Describe the morphology of the red blood cells.
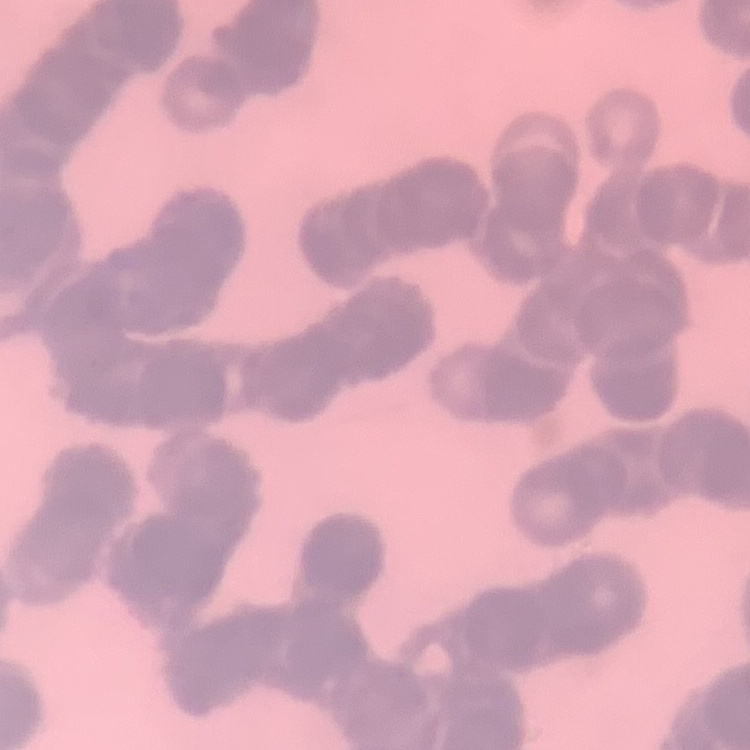
Rouleaux formation.

Square crop of a larger photomicrograph. Field's or Giemsa stain. Thin blood film.